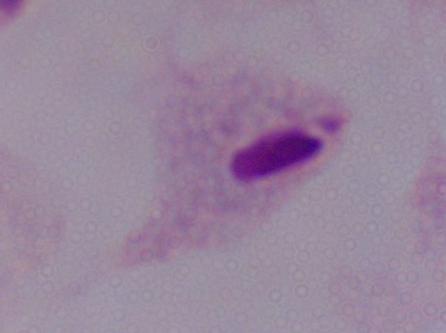
Summary:
  - Magnification: 1000x
  - Identification: trichomonad
  - Modality: micrograph